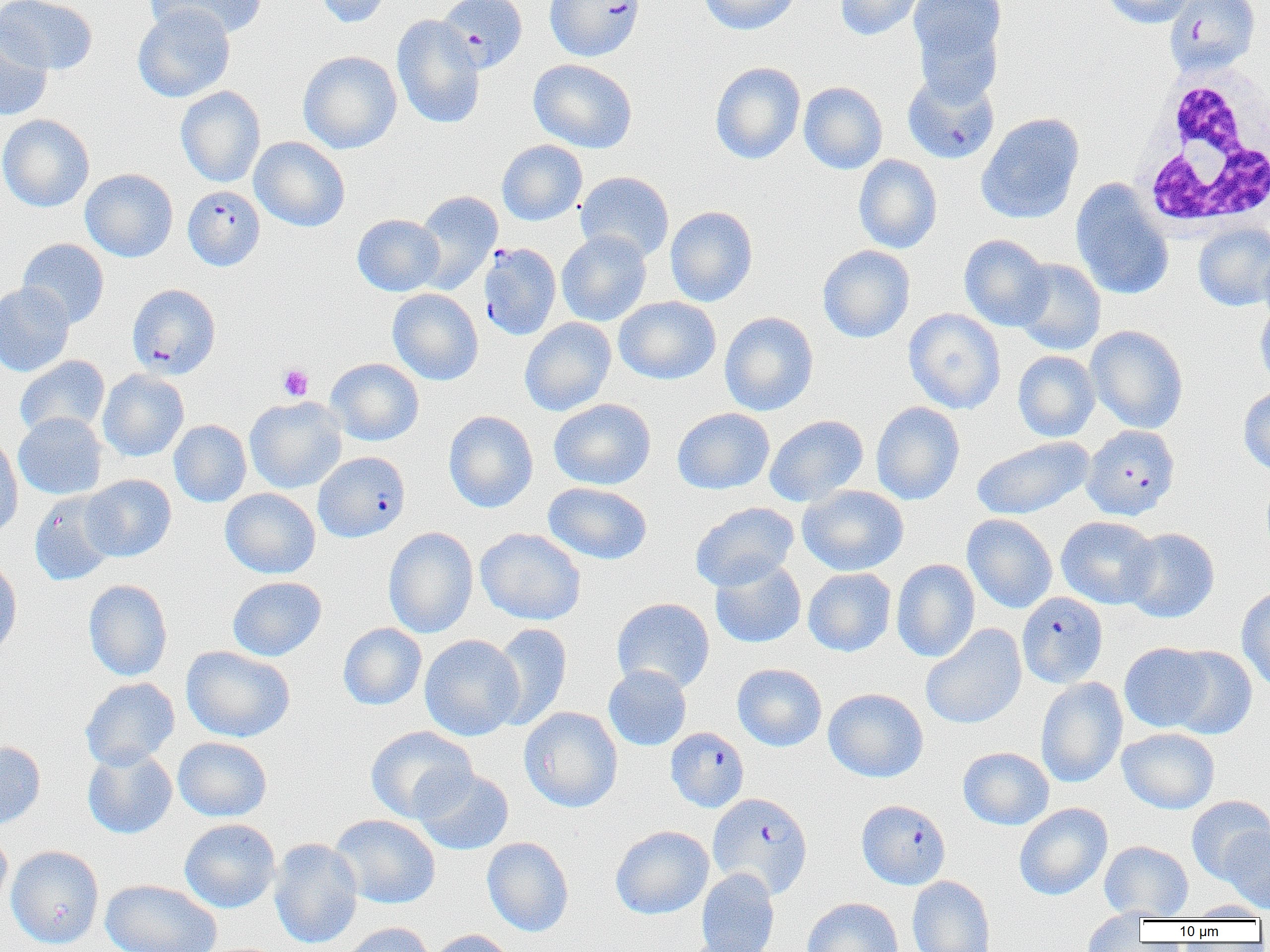
Plasmodium falciparum-infected red blood cell locations = approximate bounding boxes as (x1,y1)-(x2,y2) corner pairs in pixels: (437,0)-(527,73), (545,0)-(645,61), (1164,0)-(1260,75), (902,70)-(1000,165), (183,185)-(265,271), (478,242)-(562,341), (127,283)-(220,379), (1081,424)-(1180,520), (314,451)-(410,542), (1017,592)-(1108,688), (665,727)-(749,812), (708,793)-(812,898), (857,800)-(950,889)
slide-level diagnosis = Plasmodium falciparum
modality = light microscopy
preparation = thin blood film
platelet locations = approximate bounding boxes as (x1,y1)-(x2,y2) corner pairs in pixels: (278,364)-(313,401)
uninfected red blood cell locations = approximate bounding boxes as (x1,y1)-(x2,y2) corner pairs in pixels: (1,0)-(97,75), (146,0)-(270,40), (310,0)-(394,28), (698,0)-(801,35), (835,0)-(928,41), (909,0)-(1006,82), (1101,0)-(1196,27), (132,3)-(235,102), (391,15)-(485,129), (0,21)-(53,121), (297,50)-(402,154), (528,58)-(638,153), (710,62)-(805,164), (798,81)-(887,174), (176,85)-(266,187), (977,112)-(1084,224), (0,114)-(94,212), (250,137)-(350,231), (497,140)-(587,226), (853,154)-(942,253), (81,169)-(178,262), (575,171)-(674,263), (1071,180)-(1173,301), (414,190)-(502,294), (665,206)-(758,307), (352,214)-(445,296), (1193,222)-(1270,311), (556,230)-(652,326), (959,234)-(1052,331), (17,238)-(109,328), (817,245)-(916,343), (1258,246)-(1270,325), (1012,258)-(1106,355), (0,282)-(75,377), (387,288)-(483,385), (613,296)-(721,385), (1255,302)-(1270,391), (904,308)-(1006,414), (719,311)-(819,416), (520,317)-(616,416), (1086,325)-(1188,434), (1012,351)-(1100,442), (15,355)-(110,439), (326,358)-(424,446), (98,370)-(189,461), (1239,386)-(1270,474), (245,396)-(346,493), (549,398)-(656,490), (871,402)-(965,505), (672,407)-(775,494), (443,410)-(538,513), (13,412)-(107,500), (764,415)-(868,507), (169,420)-(251,507), (0,434)-(23,539), (971,436)-(1093,520), (81,474)-(176,562), (543,482)-(653,565), (798,484)-(909,576), (220,488)-(320,579), (29,491)-(119,586), (690,502)-(799,592), (962,514)-(1058,613), (1056,516)-(1159,609), (383,526)-(478,638), (1121,527)-(1219,623), (475,528)-(586,625), (0,554)-(22,659), (710,558)-(806,649), (892,559)-(980,662), (803,568)-(896,656), (227,576)-(326,661), (84,579)-(172,681), (1236,584)-(1270,692), (612,597)-(714,694), (338,623)-(426,710), (489,623)-(572,730), (920,624)-(1027,729), (419,634)-(524,741), (1119,642)-(1215,732), (181,645)-(295,742), (1164,645)-(1257,739), (732,663)-(827,751), (603,665)-(691,751), (80,677)-(180,770), (1035,677)-(1128,788), (823,688)-(928,782), (519,706)-(623,812), (365,726)-(476,823), (1117,727)-(1220,814), (173,737)-(273,821), (0,741)-(46,830), (82,747)-(177,839), (958,747)-(1054,830), (414,768)-(514,855), (1186,795)-(1270,883), (1014,802)-(1112,900), (329,814)-(441,909), (179,819)-(280,912), (610,825)-(714,919), (0,827)-(13,912), (1220,827)-(1270,914), (481,837)-(574,936), (269,838)-(363,949), (1099,840)-(1193,920), (6,845)-(104,949), (696,868)-(779,952), (907,875)-(996,952), (100,879)-(221,952), (802,897)-(903,952), (1185,901)-(1269,920), (1081,908)-(1149,951), (340,922)-(436,952), (429,929)-(519,952), (677,936)-(773,952)
magnification = 1000x
image size = 1270×952 pixels
field of view = one of a larger specimen
white blood cell locations = approximate bounding boxes as (x1,y1)-(x2,y2) corner pairs in pixels: (1134,64)-(1270,234)